Comment on the morphology of the red blood cells.
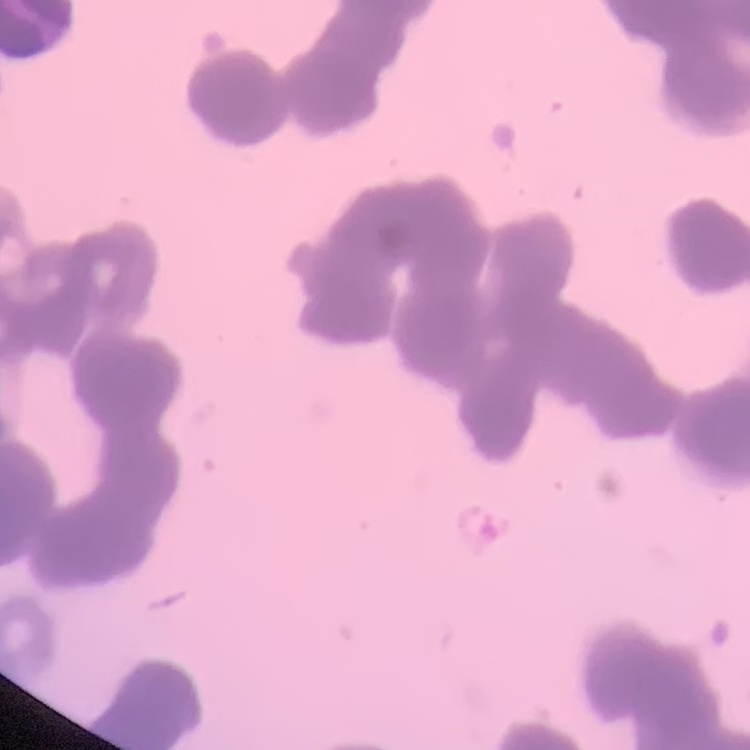
Rouleaux formation.

stain: Field's or Giemsa
image_type: square crop of a larger photomicrograph
preparation: thin blood film